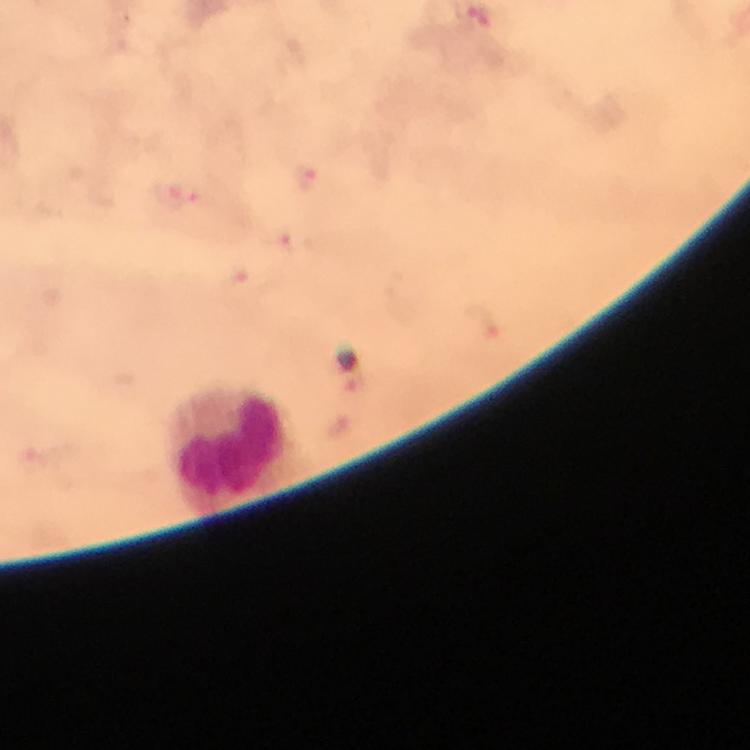
capture = smartphone camera through the microscope
immersion oil = applied
Plasmodium parasite locations = approximate centers as [x, y] in pixels: [307, 177], [183, 194], [281, 241], [238, 284], [487, 323], [356, 385]
context = from a diagnostic examination for malaria
image size = 750×750 pixels
stain = Giemsa
leukocyte locations = approximate centers as [x, y] in pixels: [227, 443]
magnification = 100x
cropped from = one field of view
preparation = thick blood smear